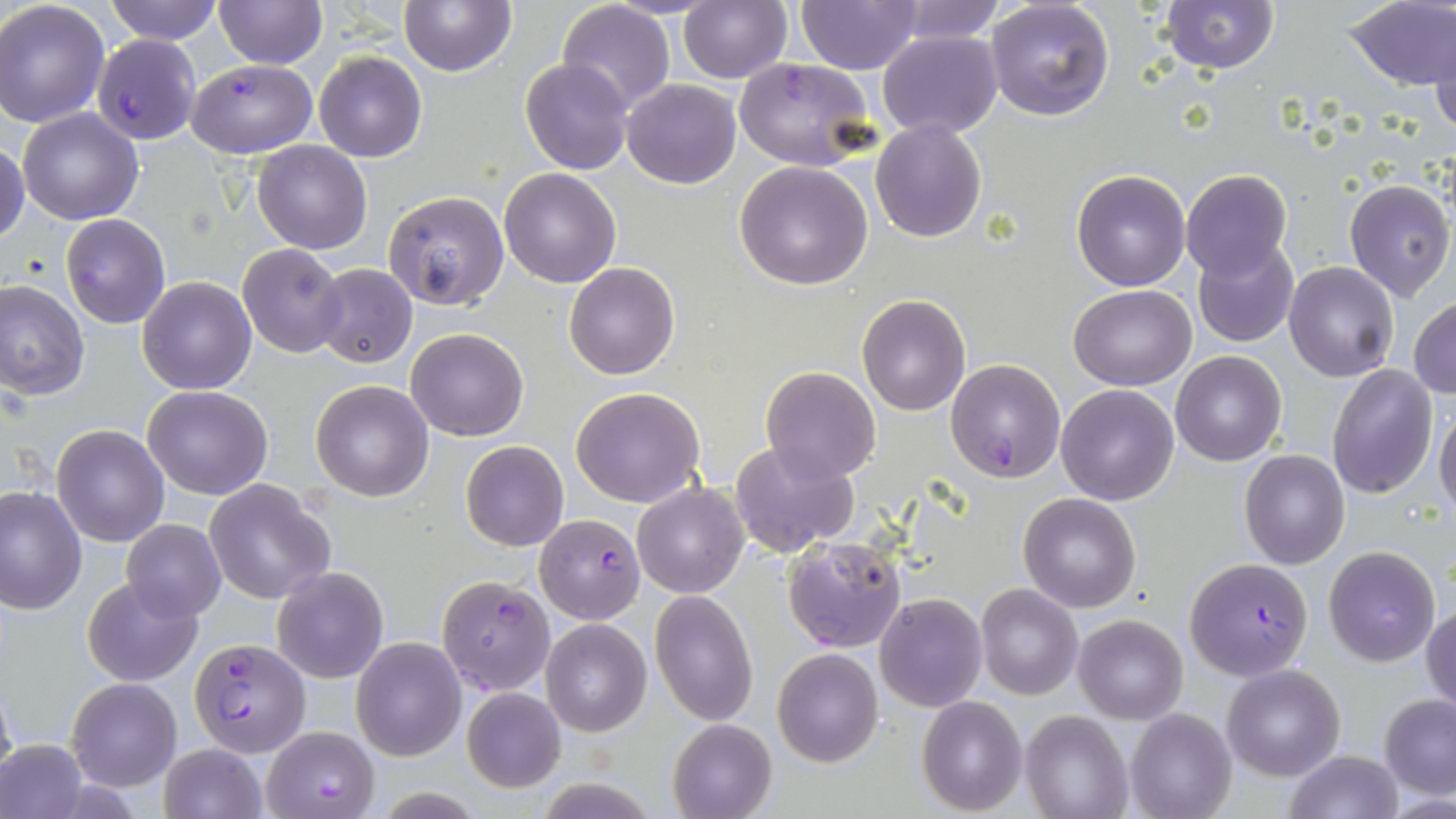

Summary:
  - Coordinate format: approximate bounding boxes as [x1, y1, x2, y2] in pixels
  - Uninfected red blood cell locations: [104, 0, 221, 44], [212, 0, 326, 69], [398, 0, 517, 75], [796, 0, 924, 73], [890, 0, 1005, 44], [985, 0, 1115, 120], [1159, 0, 1278, 73], [0, 1, 110, 128], [556, 1, 676, 114], [678, 2, 792, 83], [1345, 2, 1456, 90], [1432, 28, 1456, 136], [877, 30, 1003, 138], [313, 50, 427, 163], [520, 57, 632, 175], [622, 78, 741, 189], [17, 108, 144, 225], [870, 118, 989, 242], [252, 139, 372, 254], [0, 140, 28, 246], [734, 160, 873, 291], [498, 167, 621, 288], [1072, 169, 1190, 291], [1180, 170, 1292, 280], [1344, 178, 1453, 301], [382, 191, 509, 311], [60, 212, 170, 328], [1191, 238, 1299, 348], [238, 243, 348, 357], [564, 262, 680, 381], [1284, 262, 1400, 382], [311, 263, 418, 368], [137, 277, 256, 394], [0, 278, 88, 399], [1068, 283, 1196, 390], [856, 293, 971, 416], [1409, 297, 1456, 399], [405, 327, 529, 442], [1171, 351, 1287, 466], [760, 365, 882, 484], [1327, 365, 1438, 499], [310, 381, 434, 501], [1056, 384, 1180, 505], [143, 385, 273, 499], [571, 386, 706, 507], [1434, 404, 1456, 518], [52, 424, 169, 546], [732, 439, 857, 557], [460, 441, 568, 551], [1240, 449, 1350, 569], [203, 478, 334, 604], [632, 482, 749, 599], [1, 486, 87, 614], [1019, 493, 1141, 612], [121, 519, 226, 620], [1324, 546, 1440, 665], [271, 566, 389, 684], [81, 575, 203, 686], [977, 585, 1082, 699], [650, 590, 757, 726], [876, 592, 987, 711], [1423, 605, 1455, 716], [1074, 614, 1187, 724], [540, 618, 650, 736], [351, 637, 467, 760], [773, 649, 882, 766], [1221, 664, 1345, 780], [66, 678, 181, 791], [461, 687, 566, 792], [1380, 694, 1456, 799], [917, 695, 1028, 816], [1126, 709, 1238, 819], [1022, 711, 1133, 819], [667, 719, 778, 819], [0, 737, 86, 819], [157, 743, 266, 819], [1283, 749, 1403, 819]
  - Plasmodium falciparum-infected red blood cell locations: [94, 33, 203, 144], [734, 56, 877, 170], [185, 60, 316, 158], [947, 358, 1065, 482], [533, 513, 645, 624], [782, 537, 907, 653], [1184, 557, 1315, 680], [438, 575, 556, 696], [189, 636, 311, 757], [262, 725, 380, 819]
  - Slide-level diagnosis: Plasmodium falciparum
  - Magnification: 1000x
  - Stain: May-Grünwald-Giemsa
  - Field of view: one of a larger specimen
  - Image size: 1456×819 pixels
  - Preparation: thin blood smear
  - Modality: light microscopy